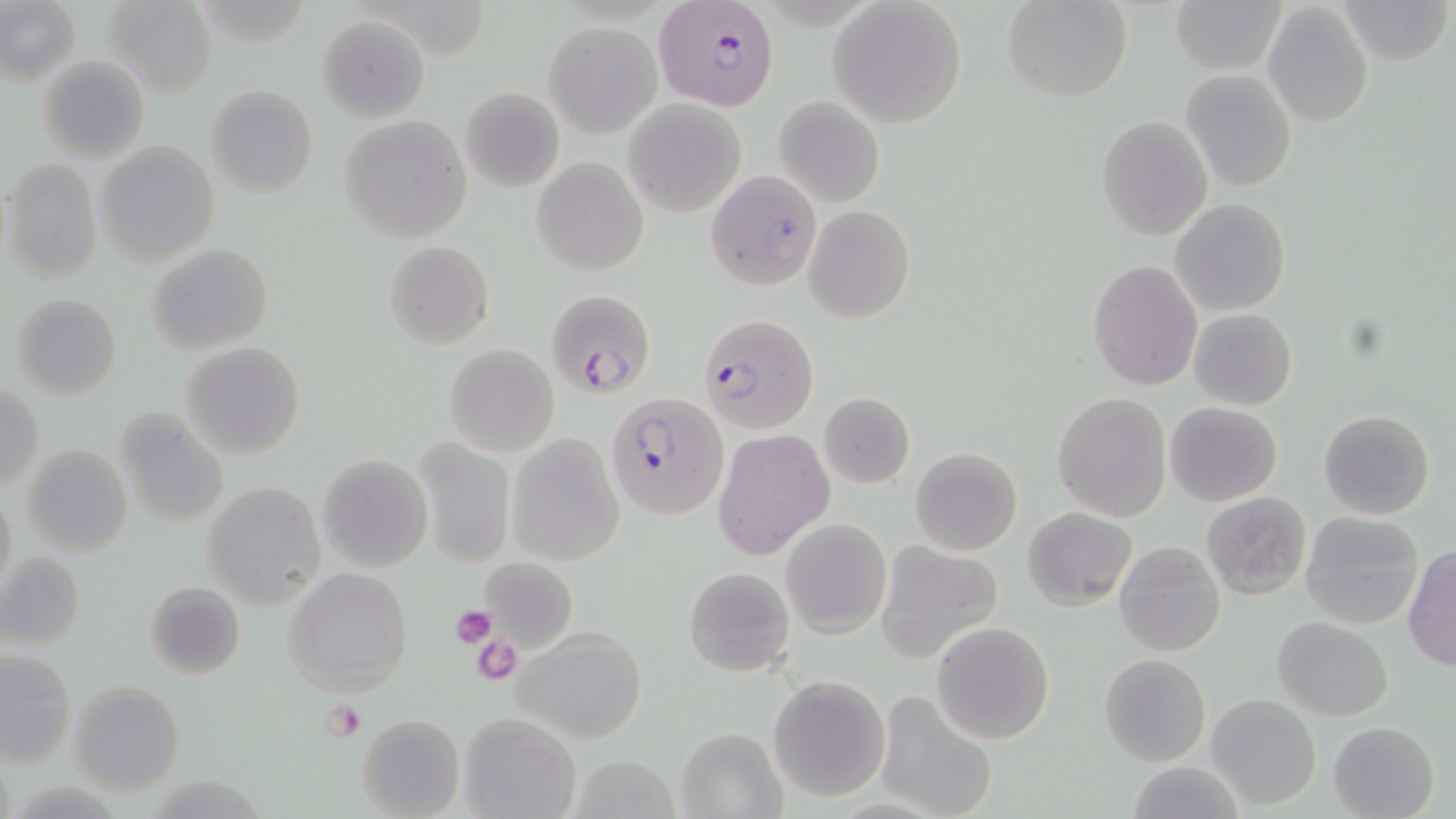
Summary:
  - Coordinate format: approximate bounding boxes as [x1, y1, x2, y2] in pixels
  - Uninfected red blood cell locations: [101, 0, 218, 97], [1003, 0, 1131, 101], [1171, 0, 1284, 74], [1335, 0, 1454, 66], [827, 1, 968, 127], [0, 2, 79, 83], [1263, 3, 1373, 130], [317, 15, 429, 122], [544, 21, 662, 138], [38, 55, 151, 164], [1180, 70, 1298, 192], [205, 84, 318, 198], [457, 86, 564, 191], [773, 95, 884, 208], [623, 99, 746, 218], [339, 115, 474, 243], [1097, 116, 1213, 240], [95, 141, 219, 266], [532, 156, 649, 276], [3, 157, 104, 282], [1170, 200, 1290, 316], [804, 205, 915, 323], [384, 241, 494, 350], [146, 243, 274, 354], [1086, 259, 1203, 392], [10, 292, 123, 399], [1188, 309, 1296, 410], [181, 341, 306, 460], [444, 345, 559, 457], [1, 382, 45, 490], [1051, 391, 1174, 522], [818, 394, 916, 488], [1164, 401, 1283, 507], [112, 407, 228, 528], [1318, 409, 1436, 521], [712, 428, 835, 558], [507, 433, 624, 565], [413, 438, 516, 568], [22, 445, 132, 557], [910, 447, 1022, 556], [317, 454, 432, 572], [1, 480, 18, 603], [201, 481, 326, 607], [1200, 492, 1313, 601], [1023, 508, 1139, 610], [1299, 511, 1424, 630], [780, 518, 892, 639], [1115, 540, 1225, 657], [874, 542, 1002, 662], [1402, 544, 1456, 672], [2, 551, 86, 652], [478, 559, 578, 652], [683, 565, 795, 678], [283, 566, 413, 697], [145, 581, 247, 679], [1271, 616, 1394, 720], [931, 621, 1055, 745], [511, 626, 647, 744], [1, 650, 75, 767], [1099, 654, 1211, 765], [766, 674, 893, 802], [68, 680, 185, 795], [873, 690, 999, 819], [1206, 693, 1320, 810], [458, 711, 580, 819], [356, 712, 465, 818], [1328, 721, 1440, 819], [675, 726, 787, 818], [566, 757, 686, 817], [1122, 762, 1242, 818]
  - Platelet locations: [449, 603, 497, 647], [472, 634, 523, 685], [325, 699, 366, 740]
  - Plasmodium falciparum-infected red blood cell locations: [654, 0, 778, 109], [704, 169, 823, 293], [544, 288, 657, 400], [698, 312, 818, 434], [606, 392, 727, 520]
  - Slide-level diagnosis: Plasmodium falciparum
  - Preparation: thin blood film
  - Magnification: 1000x
  - Modality: light microscopy
  - Field of view: one of a larger specimen
  - Image size: 1456×819 pixels
  - Stain: May-Grünwald-Giemsa